Outline each blood parasite and name the species.
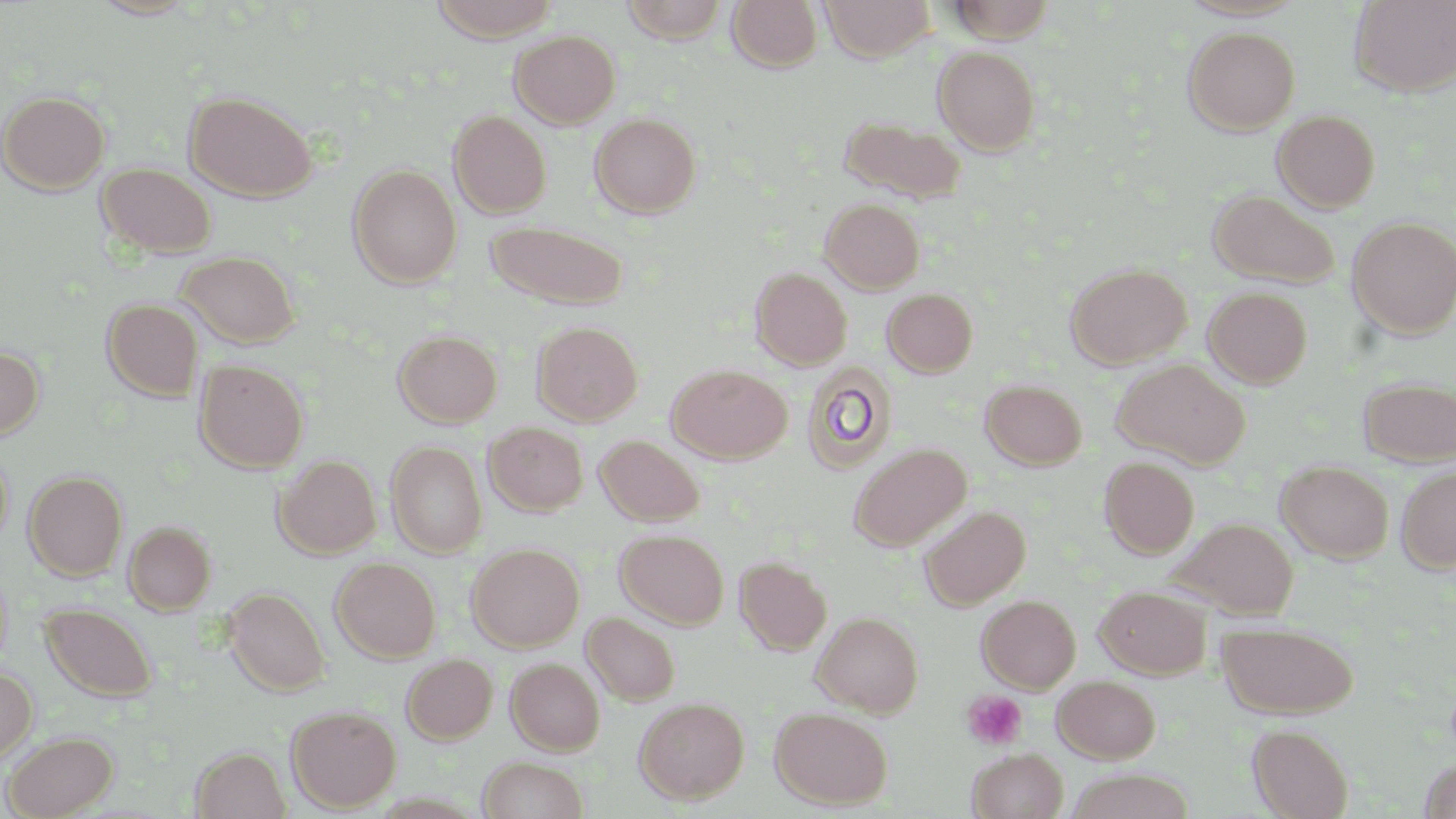
No blood parasites observed.

Summary:
  - Coordinate format: approximate bounding boxes as named x1/y1/x2/y2 corners in pixels
  - Uninfected red blood cell locations: (x1=87, y1=0, x2=202, y2=20), (x1=429, y1=0, x2=561, y2=41), (x1=618, y1=0, x2=731, y2=43), (x1=727, y1=0, x2=823, y2=72), (x1=820, y1=0, x2=936, y2=60), (x1=946, y1=0, x2=1057, y2=43), (x1=1351, y1=1, x2=1456, y2=97), (x1=1183, y1=26, x2=1301, y2=135), (x1=510, y1=29, x2=620, y2=128), (x1=932, y1=45, x2=1041, y2=154), (x1=1, y1=90, x2=110, y2=194), (x1=185, y1=91, x2=316, y2=201), (x1=1272, y1=108, x2=1381, y2=212), (x1=448, y1=110, x2=551, y2=218), (x1=590, y1=112, x2=701, y2=218), (x1=838, y1=113, x2=966, y2=203), (x1=97, y1=163, x2=216, y2=258), (x1=348, y1=164, x2=462, y2=287), (x1=1208, y1=189, x2=1340, y2=289), (x1=820, y1=197, x2=925, y2=293), (x1=1348, y1=217, x2=1456, y2=338), (x1=487, y1=220, x2=629, y2=309), (x1=176, y1=251, x2=300, y2=349), (x1=1065, y1=264, x2=1191, y2=369), (x1=750, y1=267, x2=852, y2=370), (x1=1203, y1=286, x2=1313, y2=388), (x1=882, y1=288, x2=978, y2=377), (x1=102, y1=298, x2=203, y2=401), (x1=532, y1=321, x2=643, y2=426), (x1=393, y1=330, x2=502, y2=427), (x1=0, y1=344, x2=44, y2=441), (x1=1112, y1=358, x2=1250, y2=469), (x1=194, y1=359, x2=308, y2=473), (x1=801, y1=361, x2=898, y2=473), (x1=667, y1=364, x2=791, y2=463), (x1=1358, y1=377, x2=1456, y2=465), (x1=981, y1=379, x2=1087, y2=470), (x1=484, y1=421, x2=588, y2=516), (x1=596, y1=434, x2=705, y2=527), (x1=386, y1=441, x2=487, y2=558), (x1=848, y1=442, x2=971, y2=551), (x1=0, y1=445, x2=13, y2=549), (x1=274, y1=455, x2=380, y2=558), (x1=1100, y1=456, x2=1200, y2=558), (x1=1276, y1=460, x2=1394, y2=563), (x1=1396, y1=465, x2=1456, y2=573), (x1=24, y1=470, x2=127, y2=580), (x1=919, y1=505, x2=1030, y2=609), (x1=1172, y1=516, x2=1298, y2=619), (x1=123, y1=520, x2=216, y2=614), (x1=615, y1=528, x2=729, y2=629), (x1=467, y1=543, x2=584, y2=651), (x1=735, y1=556, x2=832, y2=655), (x1=331, y1=557, x2=441, y2=662), (x1=1095, y1=584, x2=1211, y2=679), (x1=223, y1=587, x2=330, y2=695), (x1=977, y1=594, x2=1081, y2=693), (x1=41, y1=603, x2=157, y2=703), (x1=813, y1=611, x2=923, y2=716), (x1=582, y1=612, x2=680, y2=705), (x1=1219, y1=622, x2=1358, y2=718), (x1=402, y1=653, x2=497, y2=743), (x1=506, y1=658, x2=605, y2=755), (x1=0, y1=668, x2=37, y2=765), (x1=1052, y1=675, x2=1161, y2=764), (x1=634, y1=697, x2=749, y2=804), (x1=286, y1=705, x2=401, y2=812), (x1=770, y1=707, x2=893, y2=809), (x1=1248, y1=723, x2=1354, y2=819), (x1=2, y1=730, x2=118, y2=819), (x1=191, y1=746, x2=290, y2=819), (x1=968, y1=749, x2=1068, y2=819), (x1=478, y1=756, x2=588, y2=818), (x1=1420, y1=759, x2=1456, y2=818), (x1=1066, y1=770, x2=1195, y2=819)
  - Platelet locations: (x1=962, y1=690, x2=1027, y2=749)
  - Slide-level diagnosis: no evidence of blood parasites
  - Stain: May-Grünwald-Giemsa
  - Magnification: 1000x
  - Modality: light microscopy
  - Image size: 1456×819 pixels
  - Preparation: thin blood smear
  - Field of view: one of a larger specimen